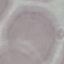

malaria_status: uninfected
preparation: thin blood smear
stain: Giemsa
capture: smartphone through the microscope eyepiece
image_type: automatically extracted cell patch, resized to 64 × 64 pixels